Assess this cell for malaria.
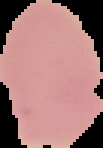
It is uninfected.

image type = segmented cell region with the area outside set to black
image size = 103×148 pixels
preparation = thin blood smear